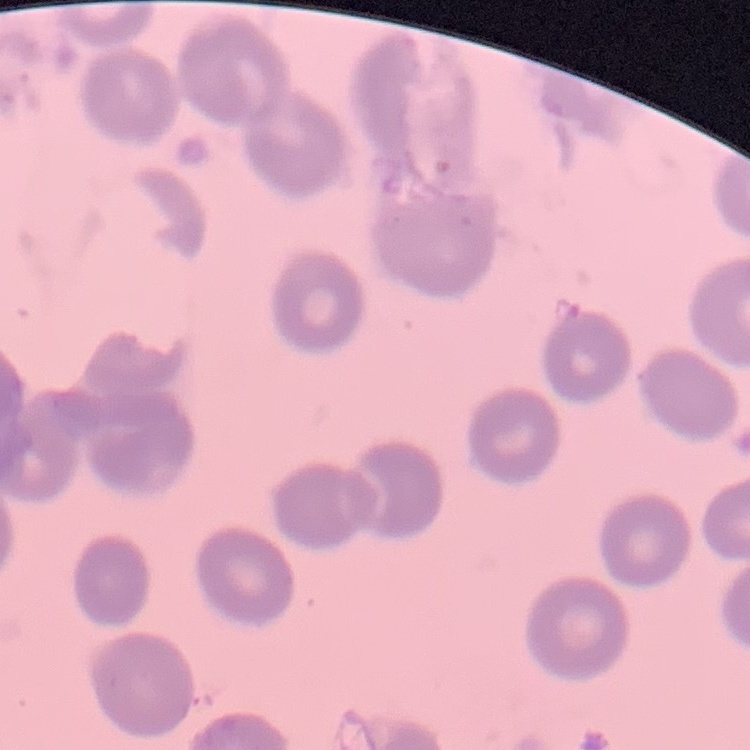

The red blood cells exhibit no rouleaux formation. Thin peripheral smear. Stained with either Field's or Giemsa. One tile cut from a larger photomicrograph.